Locate every blood parasite and identify its species.
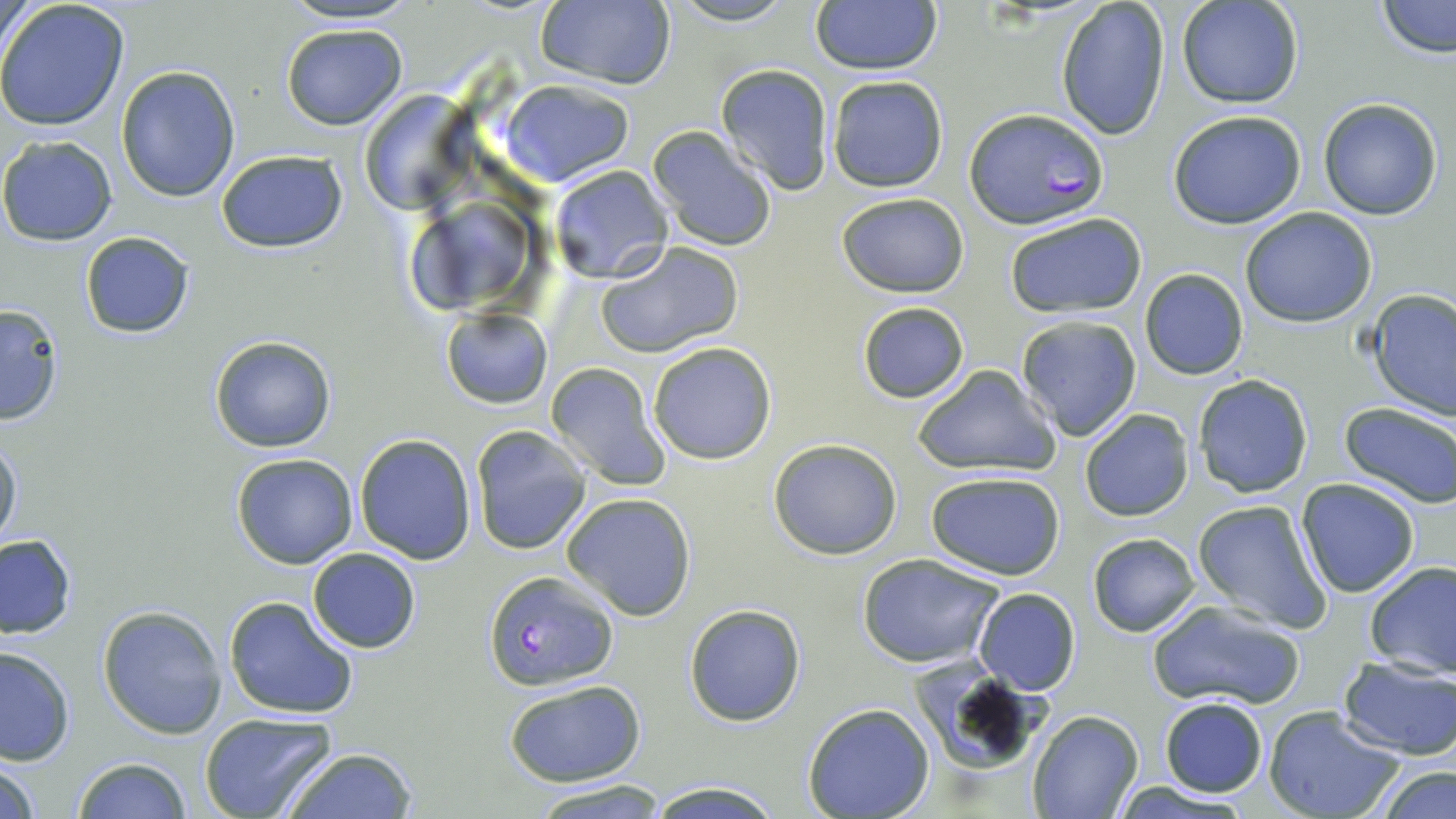
Approximate bounding boxes as [x1, y1, x2, y2] in pixels.
Plasmodium falciparum-infected red blood cells: [963, 108, 1107, 231], [483, 570, 618, 691].
No Plasmodium ovale, Plasmodium malariae, Plasmodium vivax, Babesia divergens, or Trypanosoma brucei observed.

slide-level diagnosis = Plasmodium falciparum
field of view = single
image size = 1456×819 pixels
uninfected red blood cell locations = approximate bounding boxes as [x1, y1, x2, y2] in pixels: [277, 0, 423, 27], [666, 0, 796, 26], [810, 0, 943, 75], [1178, 0, 1305, 110], [1375, 0, 1456, 58], [533, 1, 677, 89], [1056, 1, 1171, 141], [0, 2, 131, 133], [280, 23, 408, 130], [715, 64, 838, 194], [116, 66, 241, 201], [827, 75, 949, 193], [502, 79, 634, 187], [358, 90, 472, 213], [1318, 97, 1444, 220], [1167, 108, 1307, 230], [648, 127, 777, 252], [0, 136, 118, 246], [215, 148, 349, 255], [548, 164, 674, 282], [836, 191, 971, 296], [401, 195, 535, 320], [1240, 207, 1379, 328], [1003, 212, 1148, 318], [80, 231, 196, 338], [595, 241, 743, 359], [1139, 269, 1248, 381], [1368, 291, 1456, 419], [856, 300, 969, 405], [0, 302, 65, 425], [442, 307, 552, 408], [1015, 313, 1143, 439], [209, 335, 336, 453], [648, 342, 777, 464], [544, 361, 670, 492], [911, 365, 1061, 478], [1192, 375, 1314, 499], [1337, 402, 1456, 509], [1078, 408, 1195, 523], [470, 424, 594, 554], [0, 433, 23, 554], [354, 434, 477, 564], [768, 438, 903, 560], [231, 454, 359, 569], [925, 471, 1067, 580], [1295, 478, 1421, 600], [559, 491, 699, 622], [1192, 497, 1332, 634], [1087, 533, 1202, 637], [0, 534, 76, 640], [306, 548, 421, 653], [857, 552, 1006, 668], [1363, 561, 1456, 680], [973, 588, 1080, 696], [223, 595, 361, 721], [1144, 599, 1307, 711], [684, 603, 806, 726], [97, 604, 227, 739], [0, 644, 76, 766], [1337, 655, 1456, 760], [916, 664, 1051, 774], [502, 679, 645, 786], [1158, 697, 1268, 798], [802, 702, 935, 819], [1263, 707, 1407, 819], [1026, 710, 1143, 819], [199, 713, 336, 819], [277, 746, 419, 818], [0, 756, 44, 819], [71, 757, 194, 818], [1371, 764, 1456, 819], [645, 778, 784, 817], [528, 780, 667, 817], [1112, 780, 1254, 817]
modality = optical microscopy
preparation = thin blood smear
magnification = 1000x
stain = May-Grünwald-Giemsa